Name the blood parasite species.
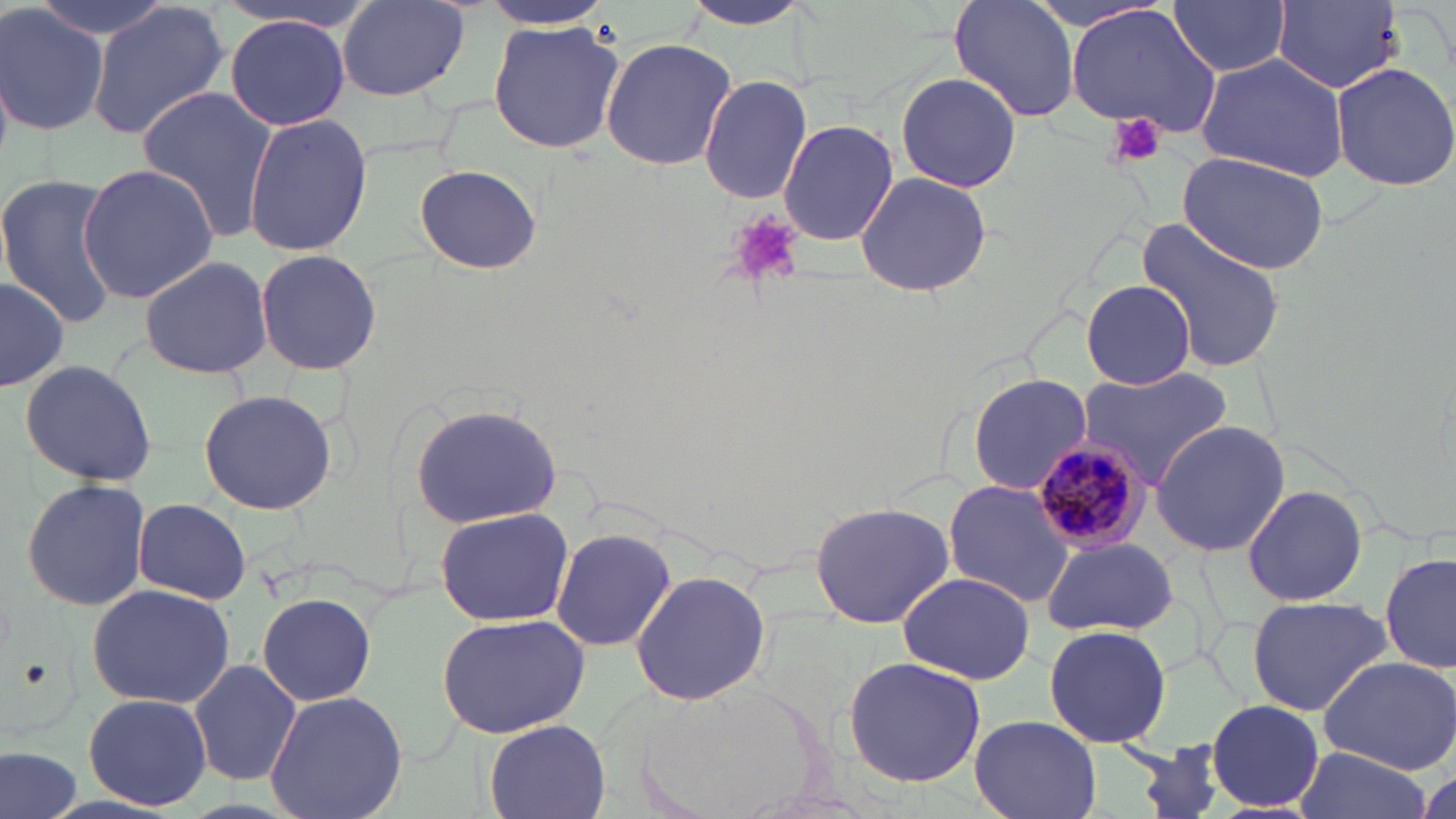

Plasmodium malariae.

Approximate bounding boxes as (x1, y1, x2, y2) in pixels. Uninfected red blood cell locations: (27, 0, 171, 41), (677, 0, 819, 33), (949, 0, 1081, 122), (472, 1, 617, 29), (1167, 1, 1293, 79), (1274, 1, 1404, 91), (336, 2, 471, 102), (0, 4, 109, 136), (86, 4, 229, 141), (1065, 5, 1220, 138), (221, 16, 354, 129), (487, 20, 626, 155), (600, 37, 737, 172), (1194, 53, 1350, 179), (1329, 62, 1456, 191), (895, 71, 1022, 192), (698, 75, 812, 204), (136, 87, 280, 242), (244, 114, 372, 257), (777, 120, 899, 246), (1178, 151, 1330, 274), (76, 163, 220, 301), (414, 163, 542, 275), (853, 171, 993, 299), (0, 175, 121, 328), (1135, 215, 1287, 375), (254, 247, 383, 375), (137, 252, 274, 380), (0, 276, 70, 390), (1081, 280, 1197, 389), (18, 357, 157, 488), (1076, 367, 1234, 493), (969, 373, 1094, 496), (197, 389, 338, 515), (409, 403, 563, 528), (1150, 418, 1290, 558), (20, 477, 153, 610), (943, 479, 1075, 607), (1242, 484, 1367, 607), (132, 499, 253, 604), (809, 500, 956, 628), (433, 507, 574, 627), (550, 528, 676, 652), (1042, 536, 1177, 637), (1381, 552, 1455, 676), (630, 569, 772, 706), (897, 572, 1035, 682), (86, 582, 236, 707), (256, 593, 376, 707), (1245, 595, 1391, 716), (434, 612, 591, 740), (1043, 624, 1173, 748), (1318, 655, 1456, 773), (841, 656, 987, 787), (189, 658, 300, 787), (638, 677, 831, 819), (263, 689, 409, 819), (82, 692, 214, 811), (1204, 701, 1325, 813), (970, 715, 1102, 819), (483, 720, 610, 818), (1117, 739, 1242, 819), (0, 744, 83, 819), (1295, 748, 1430, 819). Plasmodium malariae-infected red blood cell locations: (1029, 439, 1151, 554). Platelet locations: (1107, 112, 1167, 169), (729, 214, 805, 287). Thin blood smear. Captured at 1000x magnification. Image is 1456×819 pixels. Optical microscopy. May-Grünwald-Giemsa stain. One field of a larger specimen.